State which parasite is depicted.
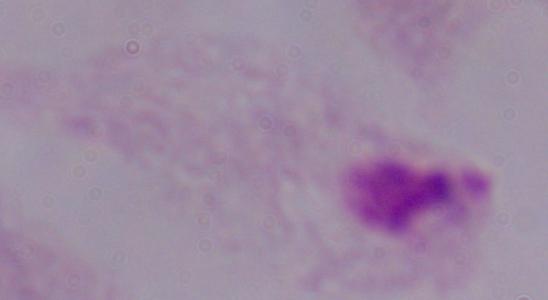

This is a trichomonad.

Summary:
  - Magnification: 1000x
  - Modality: micrograph